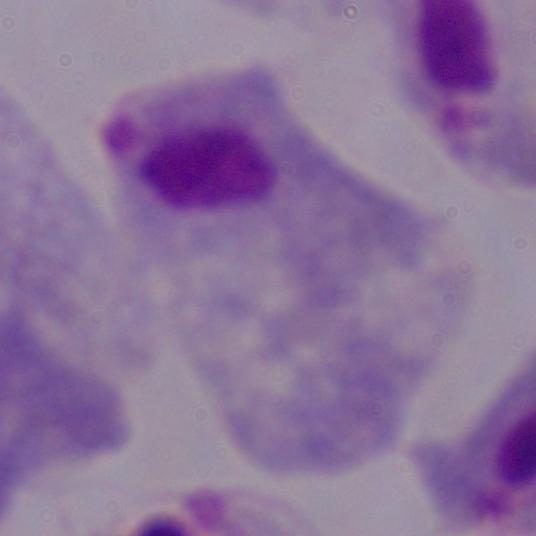

Summary:
  - Identification: trichomonad
  - Modality: photomicrograph
  - Magnification: 1000x